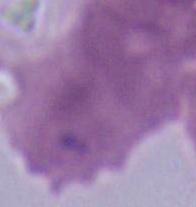

An erythrocyte is shown. Micrograph. Captured at 1000x magnification.